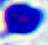
Summary:
  - Modality: micrograph
  - Identification: leukocyte
  - Magnification: 400x